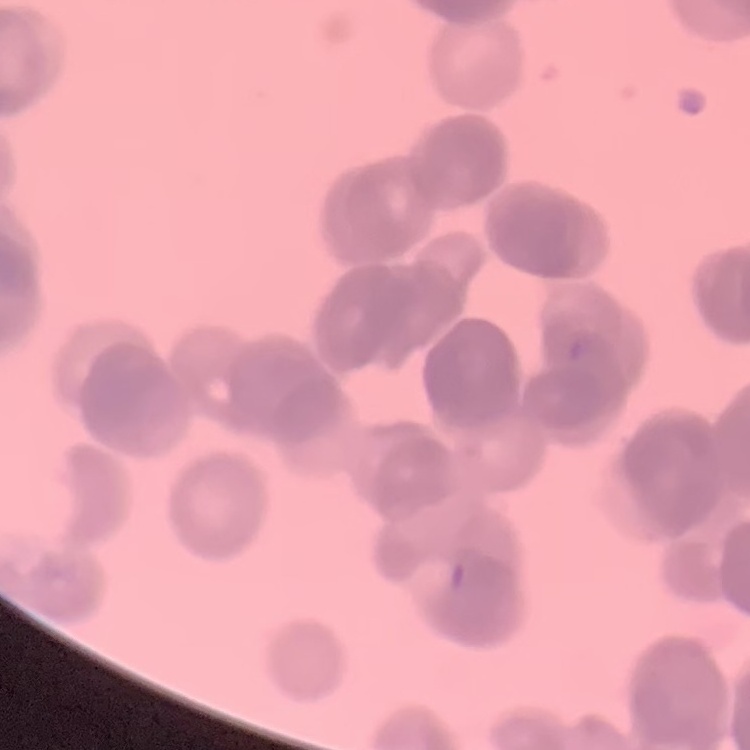
{
  "erythrocyte_morphology": "rouleaux formation",
  "preparation": "thin blood film",
  "image_type": "one tile cut from a larger photomicrograph",
  "stain": "Field's or Giemsa"
}